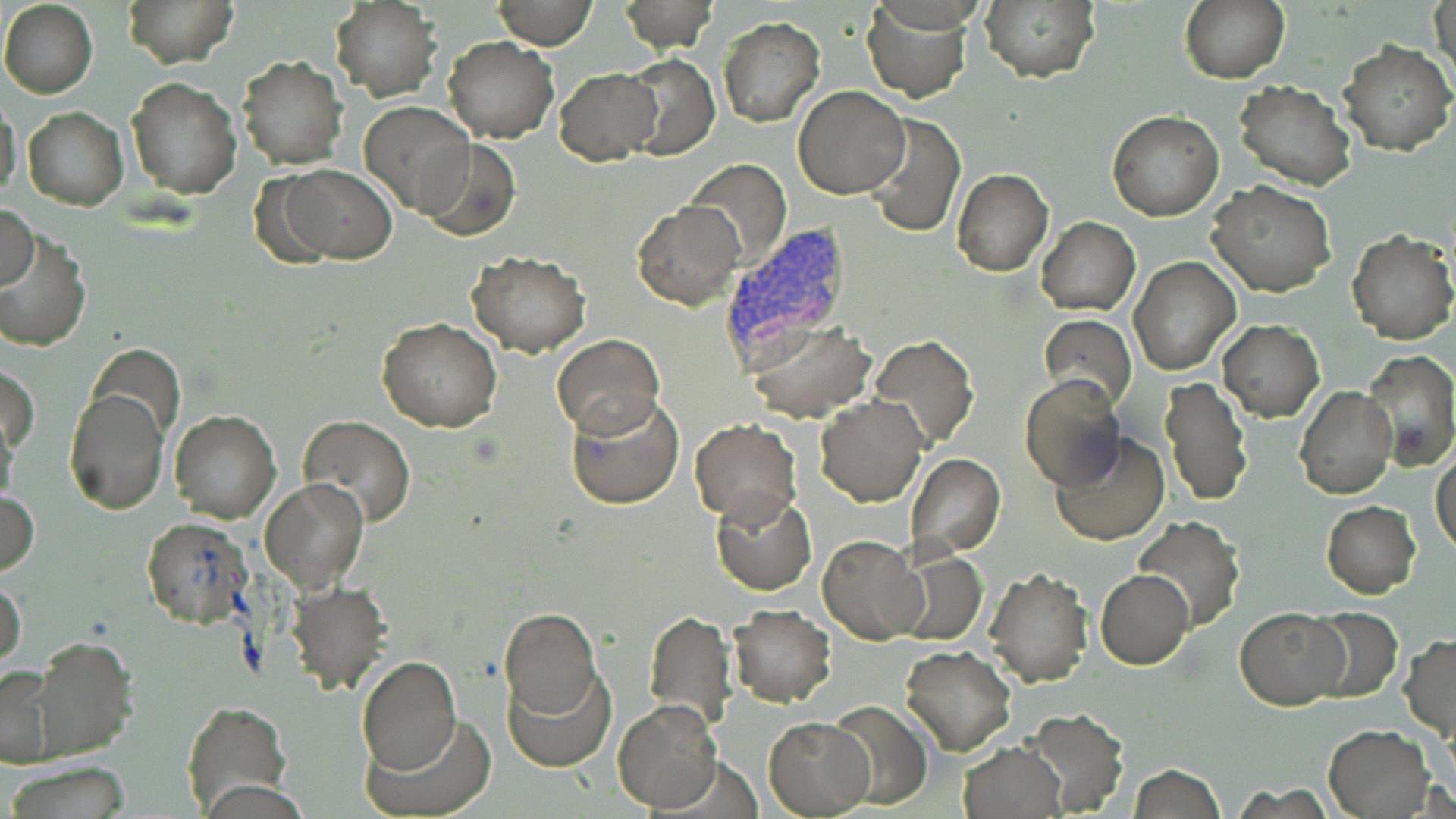

Approximate bounding boxes as [x1, y1, x2, y2] in pixels. Uninfected red blood cell locations: [0, 0, 98, 98], [124, 0, 237, 67], [495, 0, 596, 49], [618, 0, 717, 53], [861, 0, 971, 103], [1180, 0, 1289, 84], [1429, 0, 1455, 89], [978, 1, 1101, 84], [330, 2, 442, 100], [717, 16, 825, 128], [443, 35, 558, 143], [1336, 39, 1456, 155], [622, 53, 718, 160], [237, 56, 349, 170], [554, 68, 660, 165], [127, 78, 240, 199], [1233, 80, 1359, 191], [794, 85, 908, 198], [0, 93, 23, 207], [359, 101, 474, 215], [23, 106, 128, 211], [1106, 111, 1222, 221], [863, 113, 965, 237], [416, 140, 521, 242], [684, 159, 791, 270], [275, 164, 398, 264], [953, 169, 1054, 276], [1206, 181, 1336, 298], [630, 201, 744, 311], [0, 203, 38, 293], [1037, 218, 1140, 315], [1, 228, 93, 353], [1346, 230, 1456, 345], [465, 250, 591, 356], [1129, 256, 1241, 375], [1039, 313, 1137, 412], [378, 317, 503, 433], [746, 319, 877, 421], [1216, 320, 1325, 421], [551, 333, 664, 436], [868, 335, 978, 450], [90, 344, 182, 442], [1362, 350, 1456, 469], [2, 363, 38, 461], [1020, 376, 1127, 490], [1161, 377, 1253, 506], [1296, 386, 1398, 501], [63, 388, 168, 515], [565, 391, 687, 511], [814, 395, 927, 507], [1, 407, 21, 517], [169, 411, 280, 523], [298, 415, 416, 527], [690, 419, 802, 524], [1049, 431, 1171, 547], [1431, 449, 1456, 558], [905, 454, 1005, 557], [260, 478, 369, 594], [1, 487, 39, 574], [709, 490, 815, 596], [1322, 501, 1420, 599], [1133, 515, 1246, 633], [140, 516, 250, 627], [817, 535, 927, 646], [888, 547, 988, 646], [985, 566, 1093, 689], [1096, 569, 1193, 669], [0, 575, 27, 676], [284, 581, 390, 695], [728, 605, 836, 706], [1306, 606, 1402, 702], [1236, 608, 1349, 709], [499, 609, 601, 719], [645, 609, 736, 732], [1400, 634, 1456, 739], [28, 638, 137, 763], [901, 645, 1016, 756], [355, 655, 462, 774], [0, 663, 60, 768], [503, 663, 615, 770], [182, 699, 292, 815], [826, 699, 932, 809], [612, 700, 721, 812], [1022, 708, 1130, 815], [363, 715, 496, 818], [765, 717, 875, 816], [1323, 724, 1434, 818], [958, 741, 1065, 819], [3, 763, 135, 818], [1128, 765, 1226, 819]. Plasmodium vivax-infected red blood cell locations: [719, 226, 858, 368]. Slide-level diagnosis: Plasmodium vivax. Image is 1456×819 pixels. Single field of view. Optical microscopy. May-Grünwald-Giemsa-stained preparation. Captured at 1000x magnification. Thin blood smear.